Locate and identify every blood parasite.
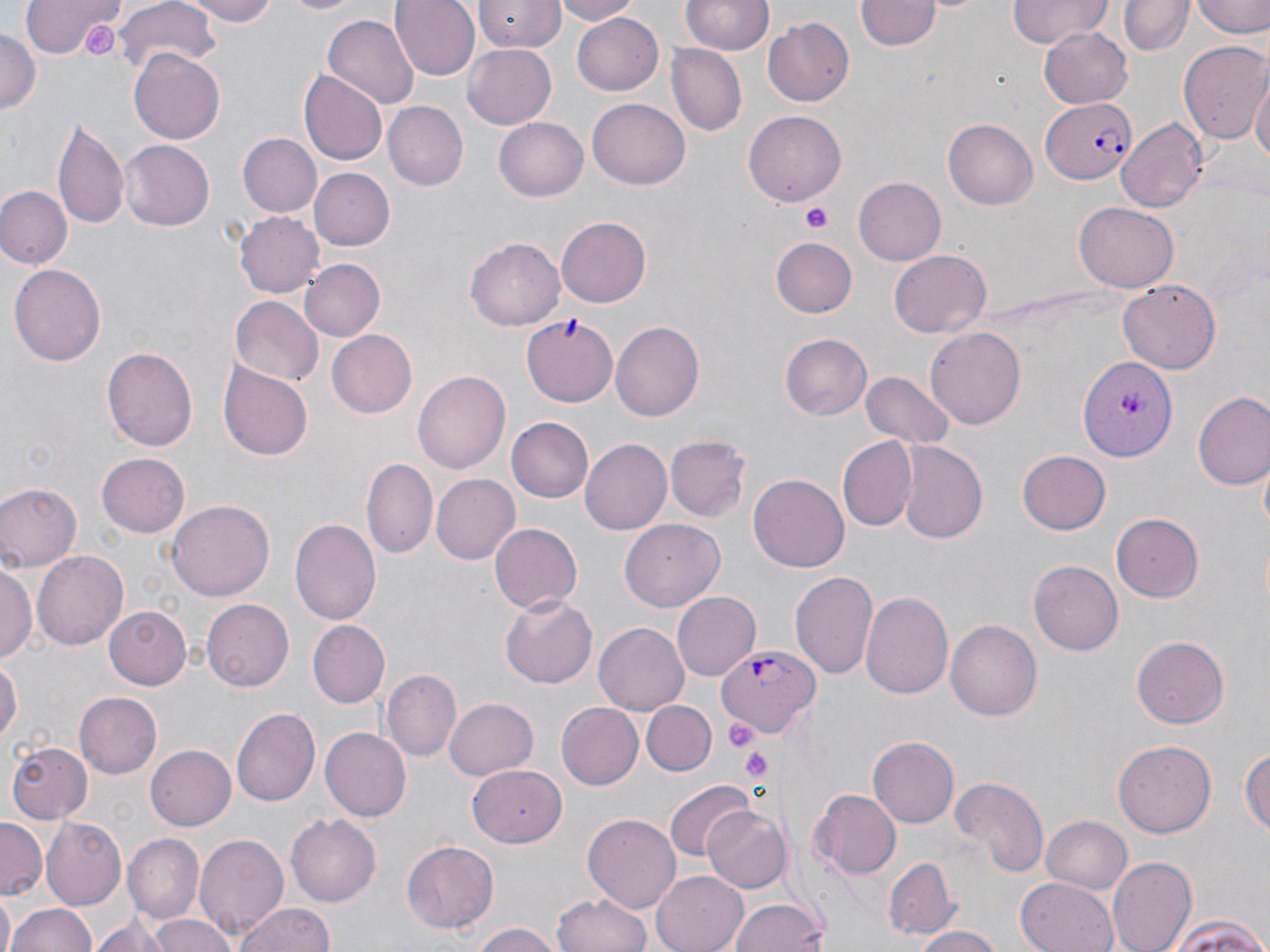

Approximate bounding boxes as (x1, y1, x2, y2) in pixels.
Plasmodium falciparum-infected red blood cells: (1041, 98, 1136, 184), (718, 644, 817, 738).
No Plasmodium ovale, Plasmodium malariae, Plasmodium vivax, Babesia divergens, or Trypanosoma brucei observed.

Summary:
  - Uninfected red blood cell locations: (20, 0, 124, 59), (179, 0, 284, 25), (279, 0, 369, 17), (391, 0, 480, 81), (475, 0, 564, 52), (550, 0, 644, 24), (1006, 0, 1113, 47), (1122, 0, 1189, 56), (1194, 0, 1270, 39), (682, 1, 773, 56), (858, 1, 939, 52), (112, 3, 220, 80), (573, 12, 664, 97), (321, 15, 418, 109), (763, 17, 855, 106), (0, 26, 40, 115), (1040, 27, 1134, 107), (1177, 40, 1269, 143), (463, 41, 556, 131), (665, 44, 746, 137), (130, 50, 226, 144), (299, 70, 387, 165), (1251, 76, 1270, 171), (588, 97, 690, 186), (381, 102, 465, 190), (742, 108, 844, 209), (53, 114, 129, 230), (492, 118, 588, 203), (943, 118, 1037, 210), (1117, 118, 1209, 213), (236, 133, 321, 218), (119, 140, 213, 230), (311, 169, 394, 249), (854, 177, 946, 265), (1, 187, 70, 269), (1075, 201, 1180, 292), (234, 210, 323, 299), (556, 215, 650, 308), (773, 236, 856, 317), (466, 237, 564, 330), (890, 249, 990, 338), (300, 257, 384, 339), (9, 262, 106, 368), (1118, 280, 1221, 373), (228, 296, 324, 388), (523, 315, 621, 405), (612, 321, 704, 421), (926, 326, 1026, 432), (327, 329, 417, 419), (779, 333, 871, 420), (103, 344, 197, 450), (1076, 357, 1177, 461), (219, 363, 314, 461), (414, 368, 509, 474), (859, 371, 955, 451), (1193, 393, 1270, 491), (504, 417, 592, 503), (666, 436, 750, 522), (580, 439, 672, 536), (838, 439, 918, 531), (899, 440, 989, 544), (98, 451, 190, 538), (1018, 451, 1111, 534), (362, 457, 437, 559), (748, 471, 849, 569), (430, 473, 519, 564), (0, 482, 82, 571), (167, 500, 275, 603), (1112, 515, 1203, 601), (290, 518, 382, 624), (621, 520, 722, 611), (488, 522, 581, 614), (33, 549, 128, 650), (1028, 559, 1125, 656), (1, 562, 36, 664), (789, 570, 878, 682), (673, 590, 761, 680), (862, 590, 954, 701), (499, 593, 598, 688), (201, 599, 293, 693), (104, 607, 192, 689), (946, 619, 1042, 720), (307, 620, 391, 707), (596, 622, 689, 713), (1132, 636, 1229, 728), (0, 657, 21, 746), (381, 669, 461, 760), (74, 692, 162, 779), (641, 694, 726, 834), (442, 698, 538, 779), (642, 701, 714, 776), (555, 702, 642, 791), (232, 708, 319, 808), (319, 727, 410, 821), (867, 737, 959, 828), (1113, 740, 1217, 837), (9, 742, 92, 822), (1241, 742, 1270, 841), (144, 743, 236, 832), (466, 766, 564, 848), (948, 777, 1047, 877), (664, 781, 756, 861), (808, 789, 902, 878), (702, 806, 791, 894), (583, 812, 683, 912), (286, 814, 381, 906), (1040, 814, 1132, 894), (43, 818, 127, 907), (0, 819, 46, 900), (193, 832, 287, 939), (123, 835, 204, 925), (402, 840, 500, 934), (1108, 855, 1195, 952), (881, 857, 957, 939), (651, 868, 751, 952), (1014, 876, 1123, 952), (553, 889, 653, 952), (0, 896, 16, 952), (728, 897, 831, 952), (9, 901, 96, 952), (233, 901, 337, 952), (93, 913, 187, 950), (141, 913, 241, 952), (1167, 915, 1270, 952), (468, 923, 566, 952), (908, 925, 1008, 952)
  - Platelet locations: (81, 17, 116, 56), (799, 202, 833, 232), (722, 716, 761, 753), (739, 747, 776, 783)
  - Slide-level diagnosis: Plasmodium falciparum
  - Image size: 1270×952 pixels
  - Stain: May-Grünwald-Giemsa
  - Field of view: single
  - Preparation: thin blood smear
  - Magnification: 1000x
  - Modality: light microscopy